Name the blood parasite species.
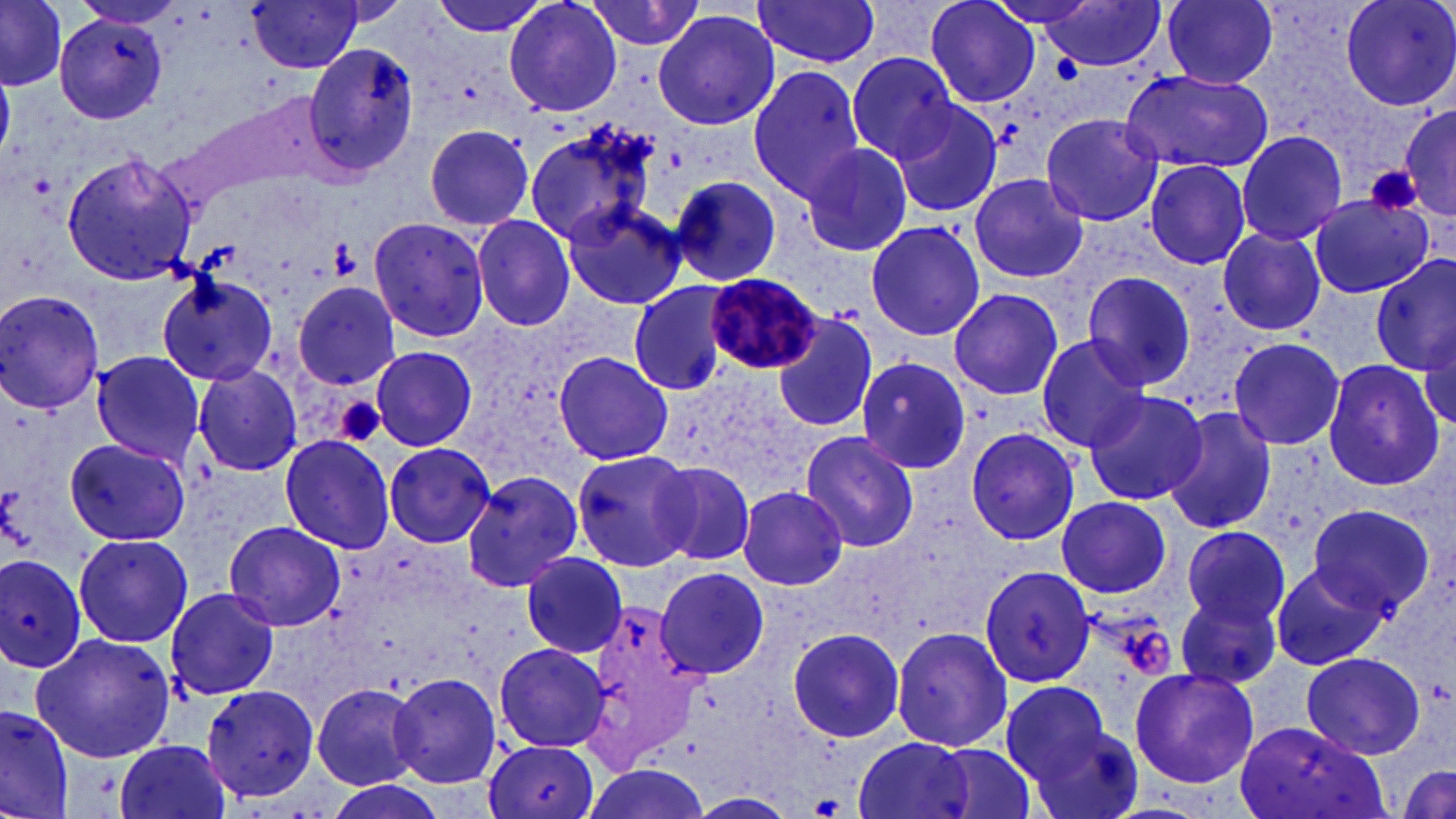

Plasmodium malariae.

magnification = 1000x
uninfected red blood cell locations = approximate bounding boxes as (x1,y1)-(x2,y2) corner pairs in pixels: (0,0)-(66,89), (245,0)-(368,74), (428,0)-(554,39), (504,0)-(622,118), (923,0)-(1042,110), (981,0)-(1106,32), (1040,0)-(1169,72), (1164,0)-(1279,89), (1337,0)-(1456,111), (585,1)-(706,51), (750,1)-(883,67), (653,8)-(780,131), (57,12)-(168,125), (303,43)-(420,175), (846,51)-(957,163), (748,65)-(871,202), (1119,68)-(1274,175), (887,100)-(1005,218), (1399,104)-(1456,224), (1042,114)-(1165,228), (523,122)-(661,247), (423,123)-(535,232), (1235,131)-(1349,246), (798,142)-(914,260), (60,153)-(198,286), (1144,158)-(1251,270), (966,172)-(1091,283), (665,173)-(785,285), (1309,194)-(1433,299), (560,198)-(688,311), (471,213)-(576,334), (365,215)-(491,343), (865,220)-(986,341), (1217,226)-(1327,337), (1372,255)-(1455,376), (1080,269)-(1197,391), (154,274)-(280,386), (627,282)-(732,395), (291,286)-(404,387), (948,287)-(1064,401), (0,290)-(107,415), (772,314)-(878,433), (1035,333)-(1154,454), (1227,338)-(1346,451), (369,346)-(477,451), (551,350)-(673,465), (89,352)-(206,464), (856,356)-(973,476), (1320,358)-(1446,491), (192,363)-(303,477), (1083,390)-(1208,505), (1162,406)-(1277,535), (964,427)-(1081,546), (799,431)-(920,550), (278,434)-(397,553), (63,438)-(191,547), (382,442)-(497,548), (570,446)-(699,573), (646,459)-(759,569), (462,468)-(590,594), (738,485)-(848,591), (1056,496)-(1172,597), (1306,503)-(1436,617), (224,519)-(345,633), (1181,526)-(1292,629), (73,533)-(191,647), (1,552)-(86,675), (522,553)-(628,658), (1271,562)-(1386,672), (979,564)-(1099,686), (657,567)-(769,678), (163,585)-(281,701), (1175,591)-(1284,692), (891,626)-(1014,752), (786,627)-(905,743), (29,632)-(177,762), (489,645)-(610,785), (1299,651)-(1427,759), (1128,667)-(1258,788), (393,674)-(502,789), (1000,680)-(1116,793), (311,682)-(427,789), (202,686)-(320,802), (1,706)-(74,817), (1029,721)-(1147,819), (1235,721)-(1392,819), (849,735)-(982,819), (114,738)-(233,819), (484,739)-(599,819), (930,741)-(1042,819), (575,762)-(709,819), (1394,765)-(1456,818), (321,777)-(444,819), (688,792)-(799,819)
field of view = one of a larger specimen
image size = 1456×819 pixels
modality = light microscopy
Plasmodium malariae-infected red blood cell locations = approximate bounding boxes as (x1,y1)-(x2,y2) corner pairs in pixels: (706,272)-(822,375)
preparation = thin blood film
platelet locations = approximate bounding boxes as (x1,y1)-(x2,y2) corner pairs in pixels: (1365,164)-(1423,217), (329,239)-(362,280), (334,395)-(386,448), (1126,623)-(1174,681), (811,795)-(843,816)
stain = May-Grünwald-Giemsa